Name the parasite shown.
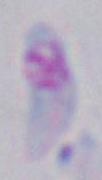

Toxoplasma gondii.

Micrograph. 1000x magnification.